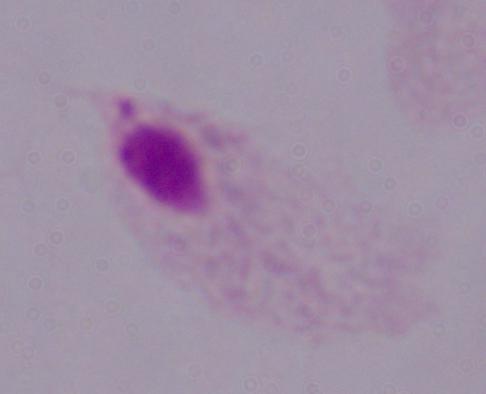
Photomicrograph. A trichomonad is seen. 1000x magnification.